Locate every malaria parasite.
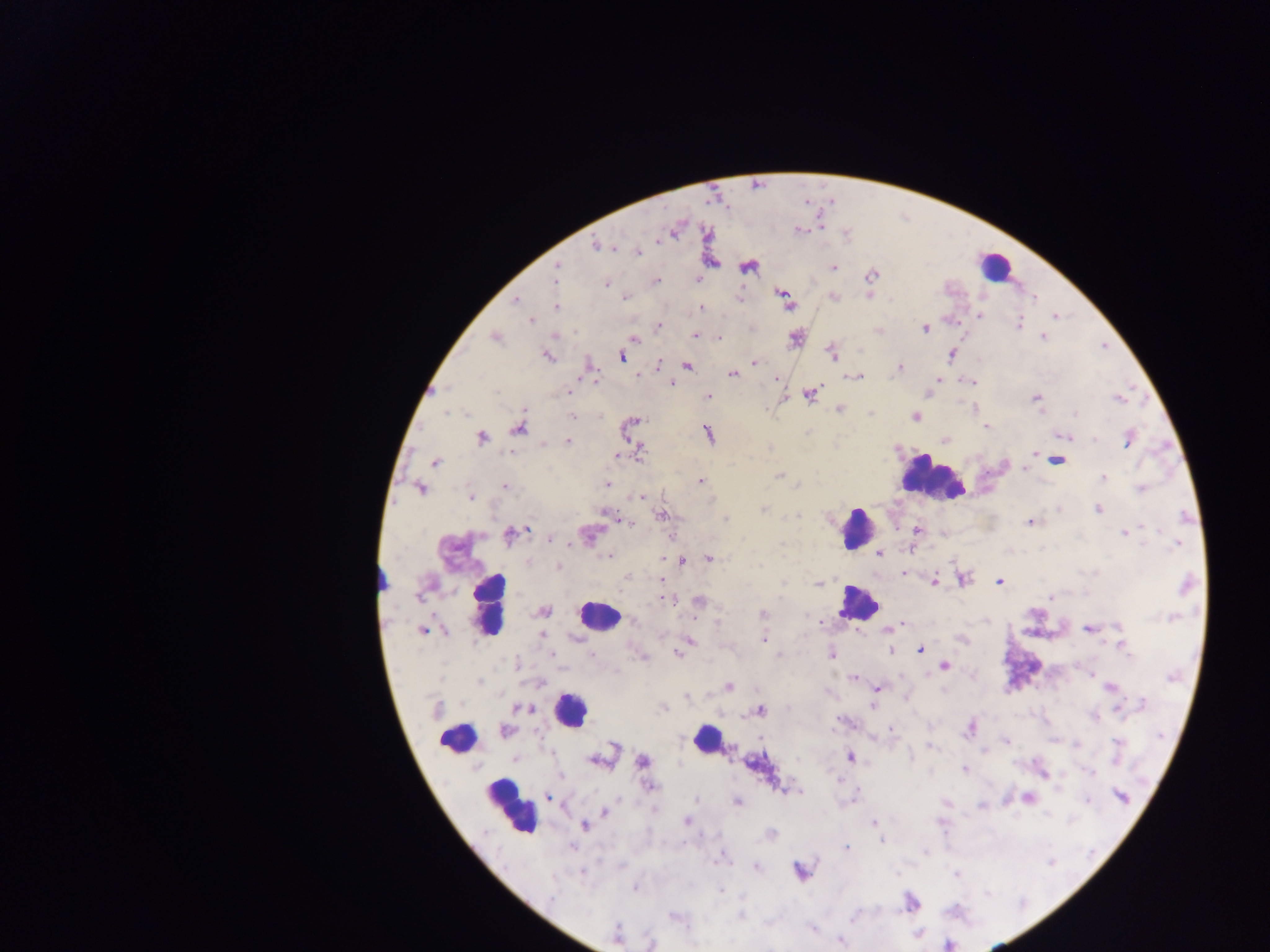

Approximate centers as {x, y} in pixels.
Malaria parasites: {675, 229}, {799, 229}, {598, 245}, {638, 252}, {711, 263}, {747, 265}, {831, 267}, {555, 273}, {870, 274}, {697, 280}, {655, 281}, {605, 283}, {784, 293}, {868, 295}, {624, 296}, {739, 296}, {832, 296}, {1034, 299}, {515, 300}, {787, 301}, {555, 307}, {702, 307}, {980, 315}, {1054, 316}, {531, 320}, {1019, 323}, {658, 326}, {924, 328}, {877, 329}, {695, 335}, {494, 337}, {633, 337}, {1043, 337}, {719, 338}, {795, 338}, {832, 352}, {547, 355}, {951, 355}, {621, 356}, {754, 362}, {658, 364}, {686, 365}, {589, 366}, {900, 368}, {731, 374}, {637, 376}, {857, 376}, {776, 379}, {939, 379}, {968, 381}, {671, 383}, {567, 391}, {809, 393}, {708, 396}, {1035, 398}, {1118, 398}, {839, 408}, {974, 408}, {572, 415}, {915, 416}, {629, 426}, {986, 426}, {519, 428}, {708, 433}, {1067, 436}, {480, 438}, {1128, 439}, {567, 440}, {945, 440}, {635, 446}, {638, 452}, {1035, 454}, {617, 455}, {1056, 460}, {434, 461}, {779, 474}, {1103, 478}, {700, 481}, {607, 485}, {503, 486}, {420, 488}, {1141, 489}, {471, 496}, {641, 496}, {1099, 509}, {764, 510}, {662, 515}, {617, 516}, {725, 519}, {1031, 521}, {917, 530}, {1125, 533}, {510, 534}, {587, 535}, {552, 538}, {911, 549}, {878, 553}, {608, 556}, {708, 558}, {681, 559}, {661, 560}, {558, 566}, {902, 574}, {627, 575}, {962, 578}, {663, 581}, {999, 581}, {819, 582}, {933, 582}, {1051, 597}, {666, 598}, {699, 601}, {542, 611}, {763, 614}, {820, 622}, {900, 624}, {887, 628}, {1089, 628}, {423, 631}, {762, 638}, {689, 641}, {1121, 645}, {919, 649}, {891, 651}, {678, 653}, {831, 654}, {780, 655}, {943, 666}, {1091, 674}, {972, 676}, {854, 677}, {728, 686}, {1110, 687}, {877, 688}, {686, 696}, {520, 707}, {663, 707}, {872, 707}, {759, 710}, {1118, 710}, {1094, 717}, {970, 728}, {891, 729}, {505, 731}, {1006, 740}, {601, 756}, {850, 757}, {642, 762}, {964, 769}, {1043, 773}, {1090, 773}, {650, 786}, {786, 790}, {548, 796}, {1120, 796}, {1027, 798}, {737, 802}, {980, 805}, {604, 811}, {686, 821}, {874, 822}, {584, 825}, {770, 833}, {882, 839}, {846, 847}, {755, 867}, {800, 870}, {957, 875}, {635, 887}, {911, 901}, {741, 915}, {675, 916}, {813, 929}, {616, 934}, {839, 941}, {650, 943}.

Leukocyte locations: {995, 266}, {932, 477}, {855, 529}, {383, 576}, {856, 603}, {490, 606}, {599, 615}, {569, 709}, {707, 738}, {456, 739}, {509, 808}. Sample from Ghana. Thick blood smear. Mobile-phone photograph taken through the microscope. Image is 1270×952 pixels. Single field of view.